Describe the morphology of the red blood cells.
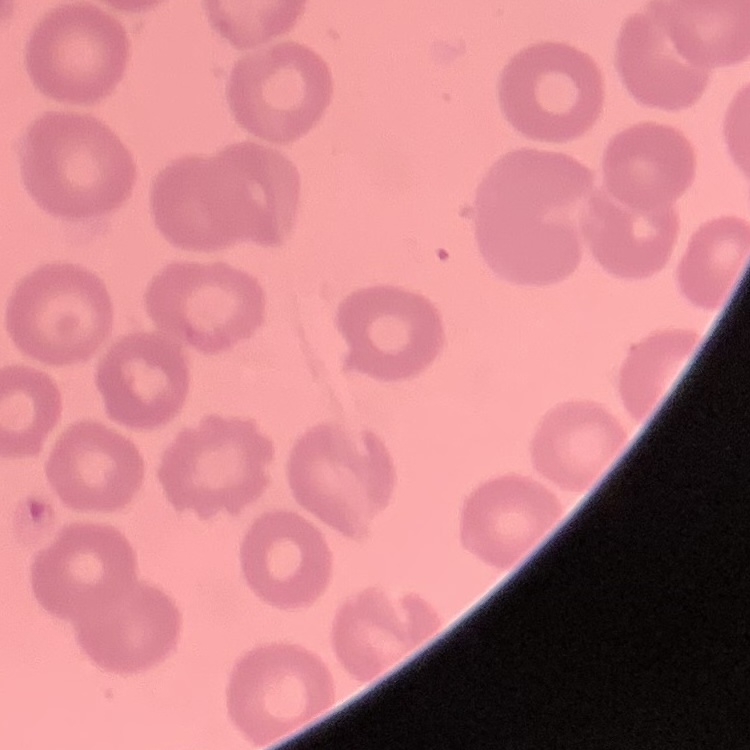

They show no rouleaux formation.

stain = Field's or Giemsa
image type = square crop of a larger photomicrograph
preparation = thin peripheral smear